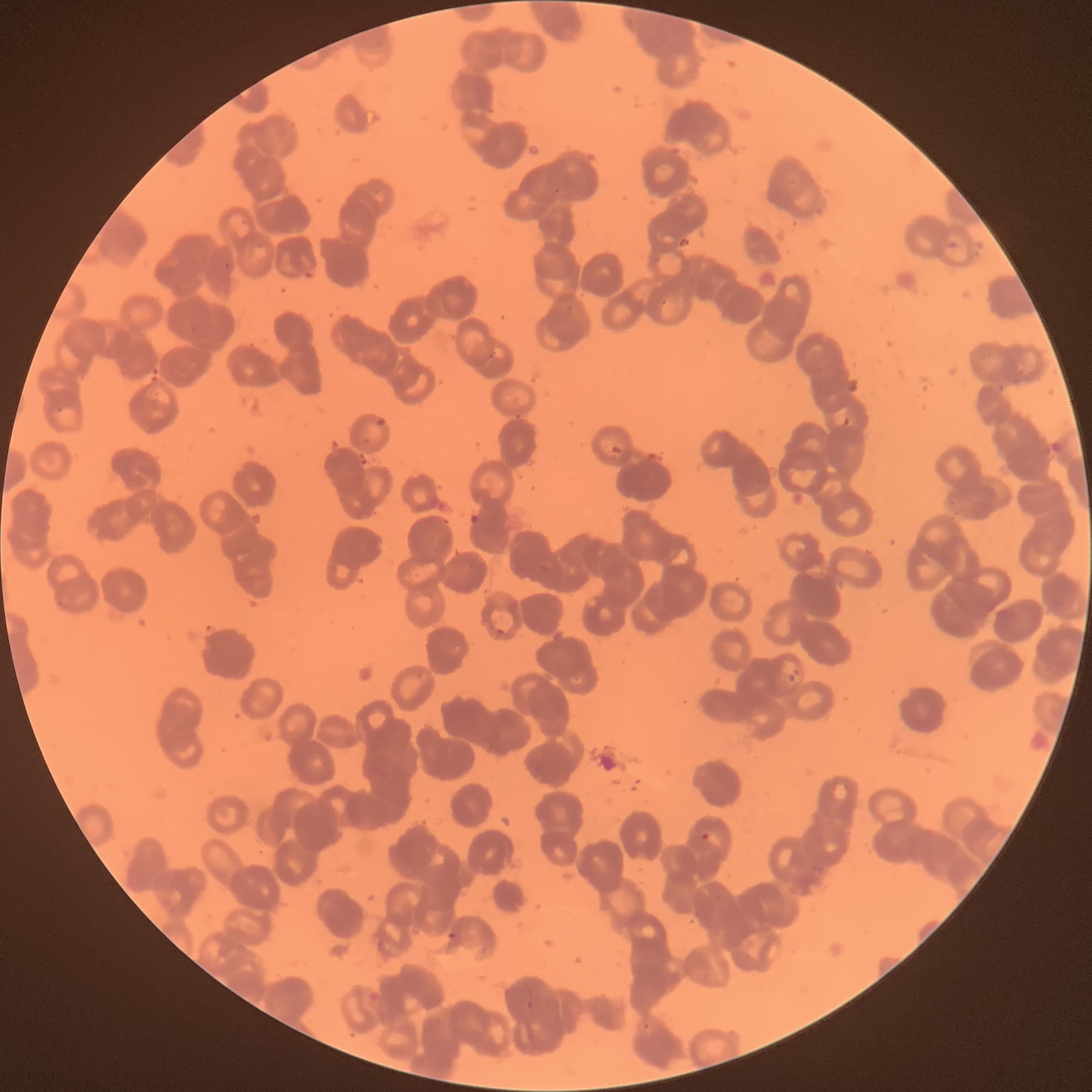 Approximate bounding boxes as (x1, y1, x2, y2) in pixels. Plasmodium parasite locations: (494, 625, 507, 636), (701, 830, 720, 848), (445, 930, 457, 942), (525, 999, 537, 1012). Image is 1092×1092 pixels. Thin blood film. The red blood cells show rouleaux formation. Optical microscopy.